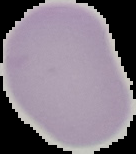

Summary:
  - Preparation: thin blood film
  - Malaria status: uninfected
  - Image size: 136×154 pixels
  - Image type: cell region segmented out of the field of view; surrounding area masked to black